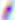
Summary:
  - Modality: photomicrograph
  - Magnification: 400x
  - Identification: Toxoplasma gondii